Locate every P. falciparum parasite and give its life-cycle stage, and locate every leukocyte and any debris.
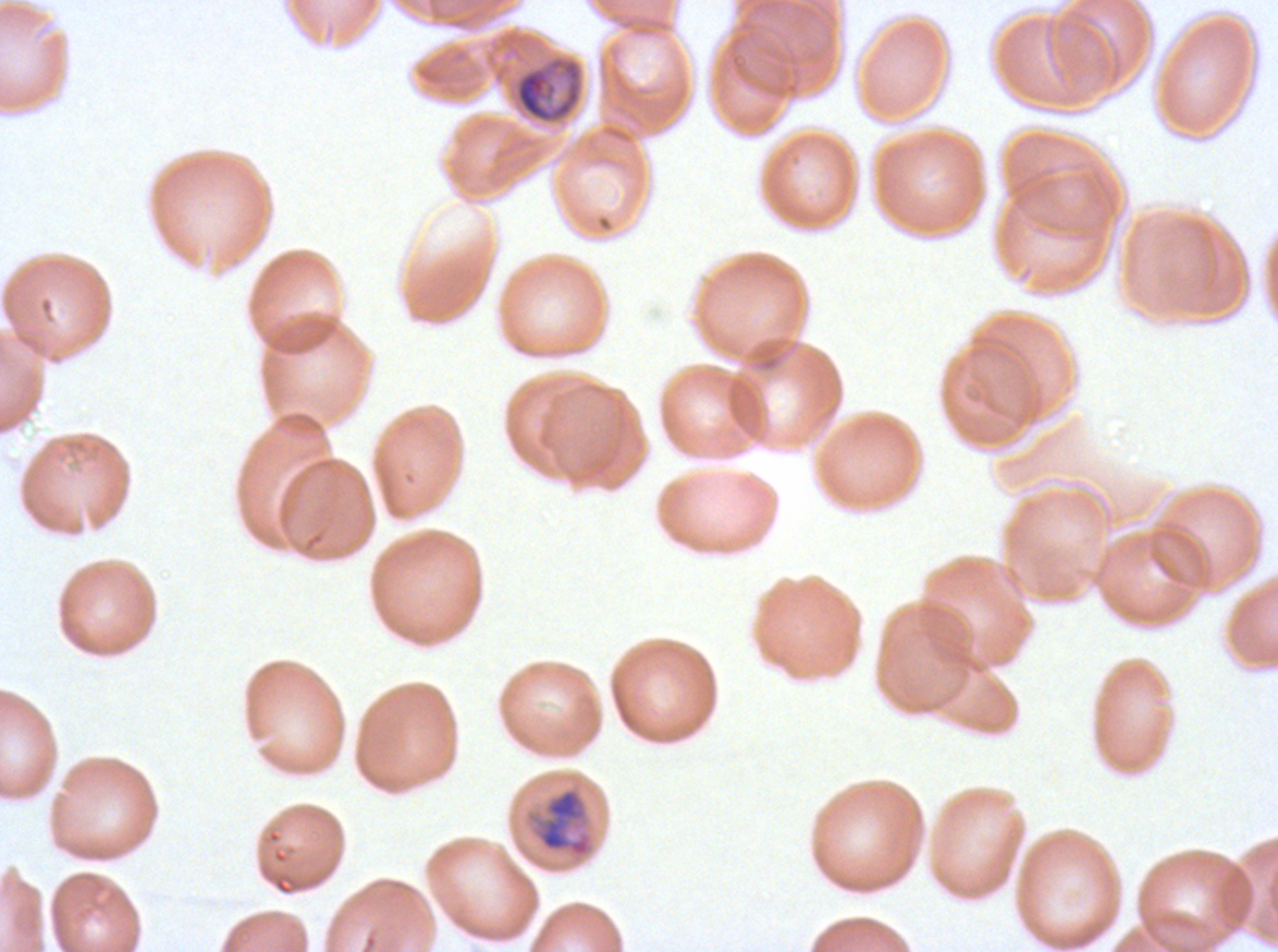
Approximate bounding rectangles given as corner coordinates in pixels from the top-left.
Mid trophozoites: (x1=514, y1=57, x2=583, y2=123), (x1=525, y1=787, x2=595, y2=860).
No rings, late-ring/early-trophozoite forms, late trophozoites, early schizonts, late schizonts, segmenters, gametocytes, leukocytes, or debris observed.

Summary:
  - Field of view: sub-image separated from a larger composite
  - Specimen: P. falciparum from a patient in The Gambia, cultured ex vivo for 24 to 48 hours
  - Image size: 1278×952 pixels
  - Stain: Giemsa
  - Preparation: thin blood film